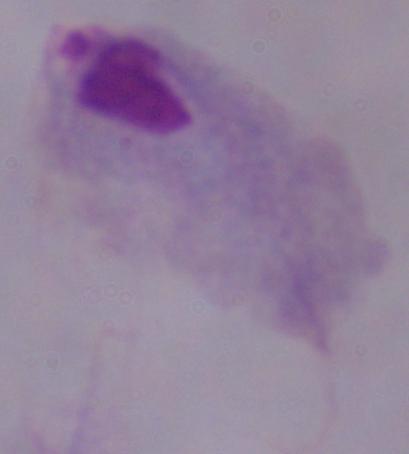 1000x magnification. A trichomonad is shown. Micrograph.